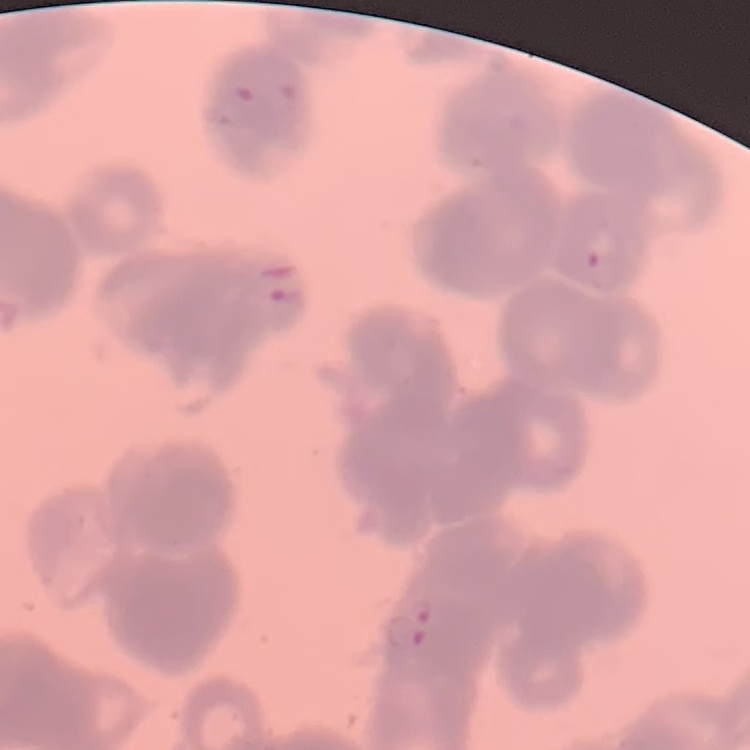
{
  "erythrocyte_morphology": "rouleaux formation",
  "stain": "Field's or Giemsa",
  "preparation": "thin peripheral smear",
  "image_type": "square crop of a larger photomicrograph"
}